Name the parasite shown.
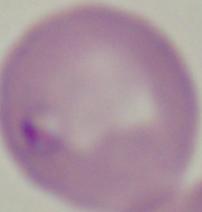
Babesia.

Summary:
  - Modality: micrograph
  - Magnification: 1000x